Comment on the morphology of the erythrocytes.
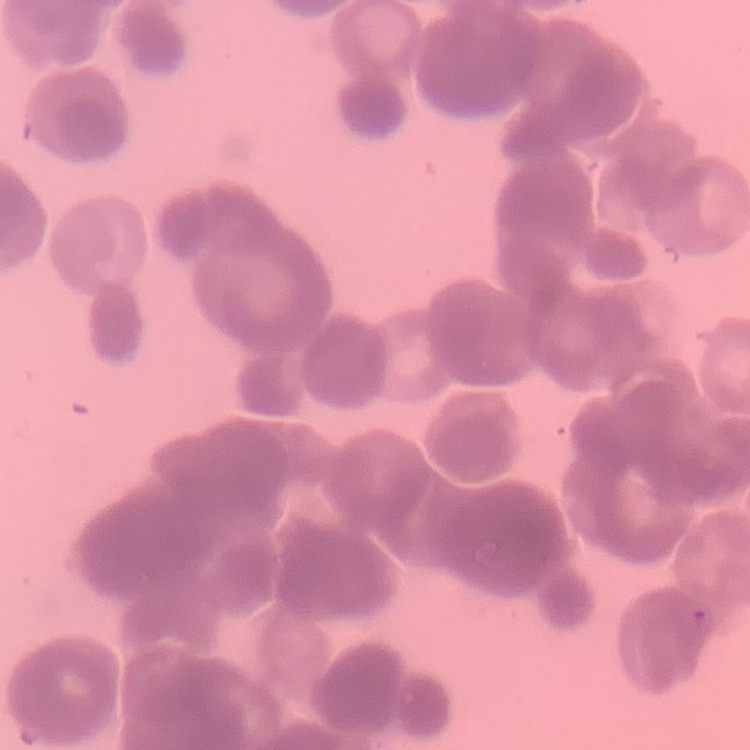
They show rouleaux formation.

Square crop of a larger photomicrograph. Thin peripheral smear. Stained with either Field's or Giemsa.